Report the malaria status of this cell.
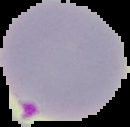

It is parasitized.

Summary:
  - Image type: segmented cell region with the area outside set to black
  - Image size: 130×127 pixels
  - Preparation: thin blood smear